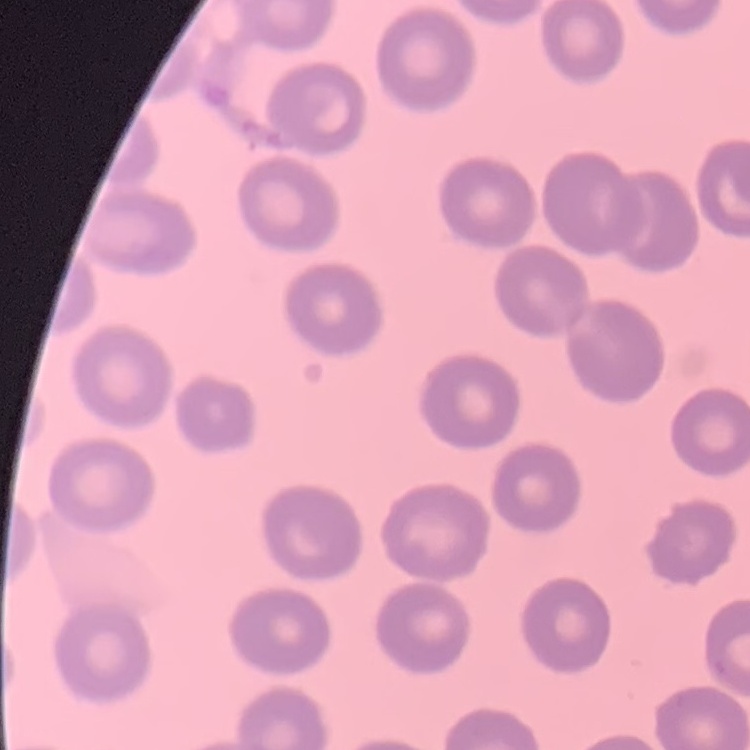

erythrocyte morphology = no rouleaux formation
preparation = thin peripheral smear
image type = one tile cut from a larger photomicrograph
stain = Field's or Giemsa